Locate every leukocyte (white blood cell).
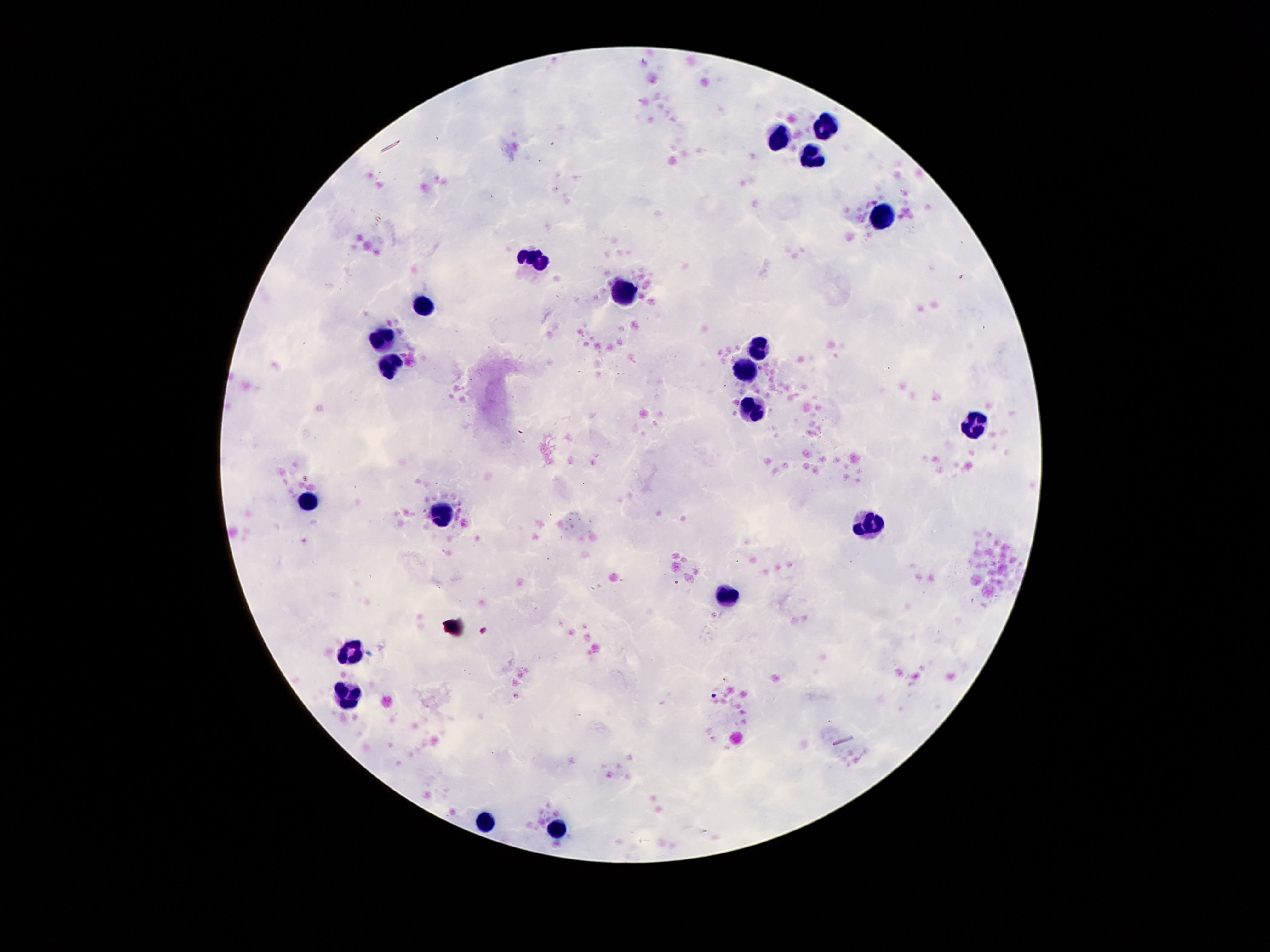
Approximate object centers, in pixels from the top-left corner.
Leukocytes: (x=824, y=126), (x=778, y=139), (x=810, y=156), (x=883, y=216), (x=536, y=257), (x=624, y=289), (x=424, y=305), (x=383, y=341), (x=758, y=347), (x=392, y=363), (x=742, y=375), (x=756, y=406), (x=973, y=426), (x=304, y=503), (x=442, y=510), (x=869, y=525), (x=728, y=594), (x=352, y=653), (x=347, y=692), (x=486, y=823), (x=560, y=826).

stain = Giemsa
capture = smartphone camera through the microscope eyepiece
preparation = thick blood film
magnification = 100x
image size = 1270×952 pixels
field of view = single
patient malaria status = not infected